Report the malaria status of this cell.
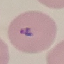

It is parasitized.

Photographed with a smartphone camera at the microscope eyepiece. Automatically extracted cell patch, resized to 64 × 64 pixels. Giemsa-stained preparation. Thin blood film.